Locate every leukocyte (white blood cell).
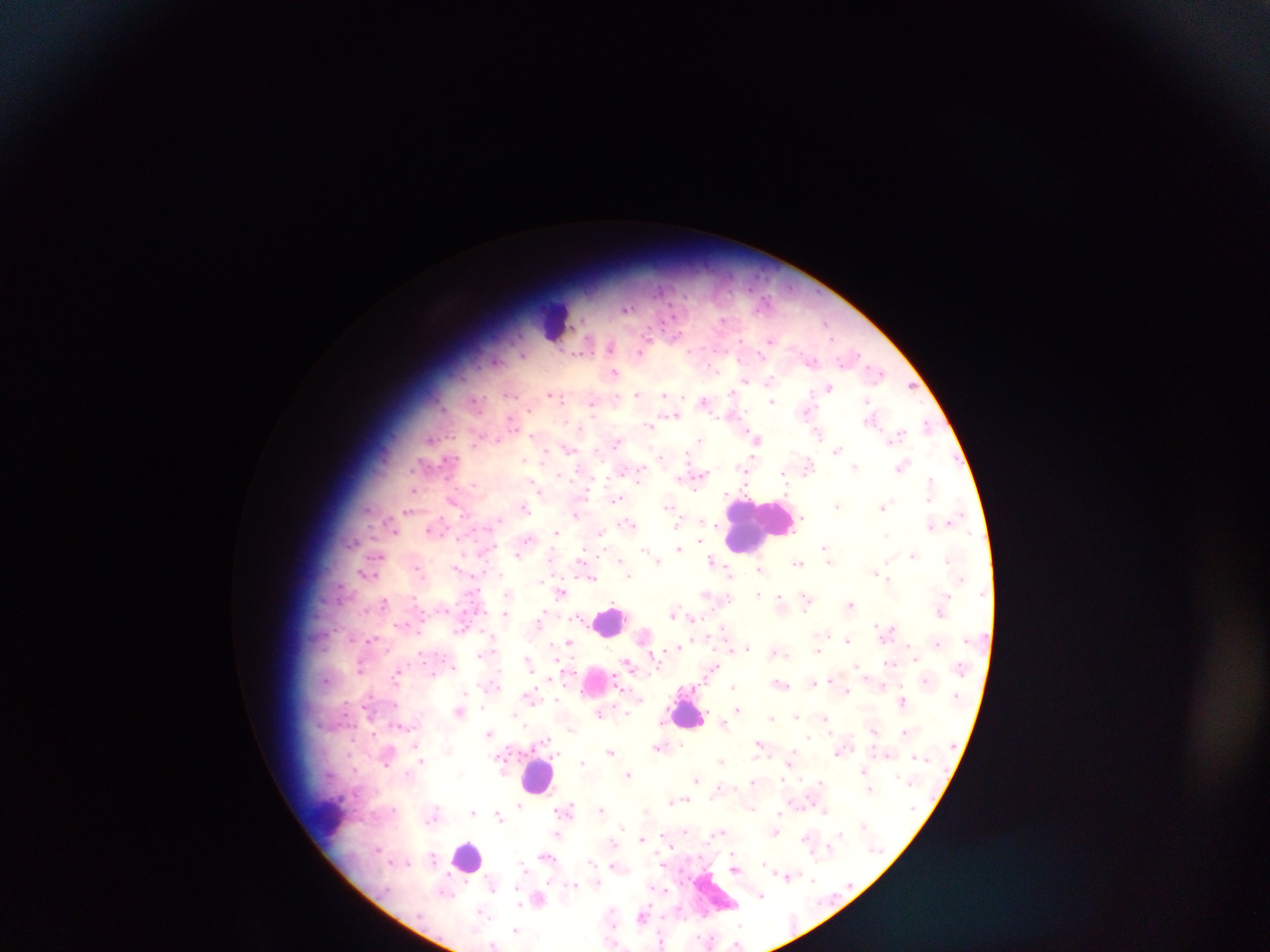

Approximate centers as {x, y} in pixels.
Leukocytes (some below the resolvable threshold): {557, 323}, {758, 524}, {611, 620}, {598, 684}, {687, 714}, {539, 774}, {331, 823}, {467, 855}.

Malaria parasite locations: {627, 308}, {723, 320}, {826, 323}, {770, 340}, {611, 346}, {642, 351}, {523, 355}, {811, 361}, {614, 372}, {876, 373}, {745, 380}, {770, 381}, {912, 386}, {829, 387}, {733, 392}, {510, 393}, {637, 393}, {550, 394}, {665, 395}, {561, 399}, {475, 400}, {704, 400}, {772, 401}, {867, 402}, {592, 403}, {806, 411}, {673, 416}, {511, 421}, {650, 426}, {928, 426}, {580, 429}, {818, 433}, {532, 436}, {896, 436}, {430, 438}, {699, 439}, {757, 439}, {497, 440}, {617, 442}, {837, 448}, {569, 450}, {546, 453}, {660, 456}, {741, 466}, {902, 466}, {808, 467}, {855, 467}, {638, 473}, {701, 475}, {784, 475}, {930, 481}, {474, 484}, {536, 487}, {413, 490}, {618, 499}, {452, 501}, {838, 505}, {524, 506}, {667, 507}, {883, 507}, {367, 508}, {408, 511}, {576, 515}, {955, 518}, {802, 520}, {497, 521}, {702, 521}, {629, 524}, {931, 527}, {429, 529}, {395, 532}, {556, 532}, {601, 532}, {886, 536}, {527, 539}, {679, 549}, {825, 549}, {646, 551}, {651, 554}, {518, 555}, {913, 555}, {377, 556}, {828, 556}, {621, 560}, {656, 560}, {948, 560}, {582, 561}, {887, 561}, {714, 562}, {798, 563}, {457, 567}, {760, 569}, {419, 571}, {875, 572}, {730, 573}, {366, 574}, {628, 574}, {592, 578}, {889, 579}, {561, 592}, {508, 594}, {759, 594}, {706, 595}, {728, 598}, {780, 599}, {806, 599}, {384, 601}, {851, 604}, {674, 612}, {505, 614}, {691, 619}, {539, 620}, {877, 624}, {461, 628}, {888, 630}, {847, 639}, {371, 641}, {569, 642}, {937, 644}, {746, 648}, {817, 651}, {781, 654}, {914, 654}, {480, 655}, {527, 662}, {890, 663}, {627, 664}, {858, 665}, {453, 666}, {360, 668}, {713, 668}, {396, 673}, {432, 674}, {325, 679}, {832, 679}, {926, 680}, {813, 683}, {780, 684}, {882, 685}, {732, 686}, {846, 691}, {465, 693}, {530, 697}, {902, 702}, {737, 708}, {458, 712}, {598, 713}, {626, 713}, {514, 715}, {795, 715}, {771, 717}, {825, 719}, {724, 722}, {401, 726}, {571, 729}, {874, 729}, {905, 732}, {374, 733}, {490, 733}, {809, 737}, {545, 740}, {758, 743}, {417, 744}, {659, 747}, {840, 750}, {611, 752}, {556, 753}, {887, 755}, {501, 758}, {421, 760}, {581, 761}, {721, 761}, {790, 762}, {386, 764}, {863, 771}, {408, 774}, {459, 774}, {629, 774}, {696, 779}, {820, 781}, {752, 782}, {870, 790}, {682, 800}, {671, 801}, {520, 806}, {394, 809}, {567, 809}, {601, 809}, {752, 809}, {473, 811}, {824, 811}, {779, 813}, {499, 815}, {433, 817}, {863, 824}, {622, 826}, {775, 830}, {685, 831}, {718, 833}, {840, 833}, {557, 834}, {804, 838}, {641, 839}, {611, 843}, {829, 848}, {733, 854}, {545, 857}, {434, 858}, {591, 862}, {764, 862}, {611, 865}, {523, 866}, {735, 869}, {788, 875}, {812, 879}, {574, 884}, {492, 885}, {761, 896}, {538, 900}, {611, 909}, {482, 912}, {642, 915}, {611, 921}, {740, 924}, {613, 925}, {515, 929}, {661, 942}, {493, 944}, {736, 944}. Single field of view. Thick blood smear. Photographed through a microscope with a mobile-phone camera. Sample from Ghana. Image is 1270×952 pixels.